Draw a bounding box around every parasitised red blood cell.
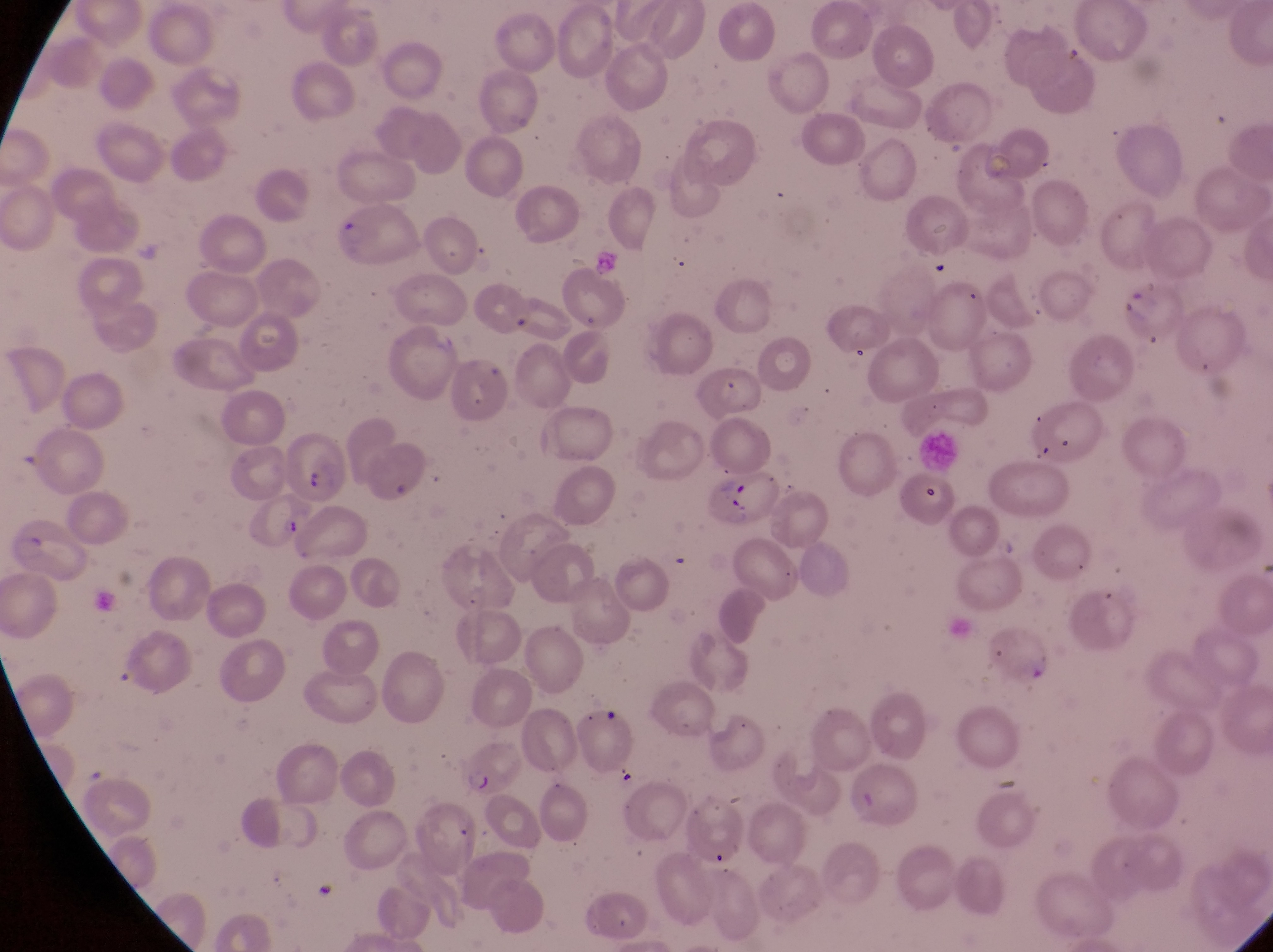
Approximate bounding boxes as [left, top, right, bottom] in pixels.
Parasitised red blood cells: [324, 202, 417, 267], [285, 425, 352, 507], [708, 469, 790, 534], [460, 737, 530, 794].

Summary:
  - Artifact (platelet-like body, stain precipitate, or debris) locations: [616, 766, 641, 796]
  - Country: Uganda
  - Magnification: 1000x
  - Preparation: thin blood film
  - Image size: 1273×952 pixels
  - Field of view: single
  - Capture: smartphone photograph through the eyepiece of an Olympus CX-23 microscope